Outline each blood parasite and name the species.
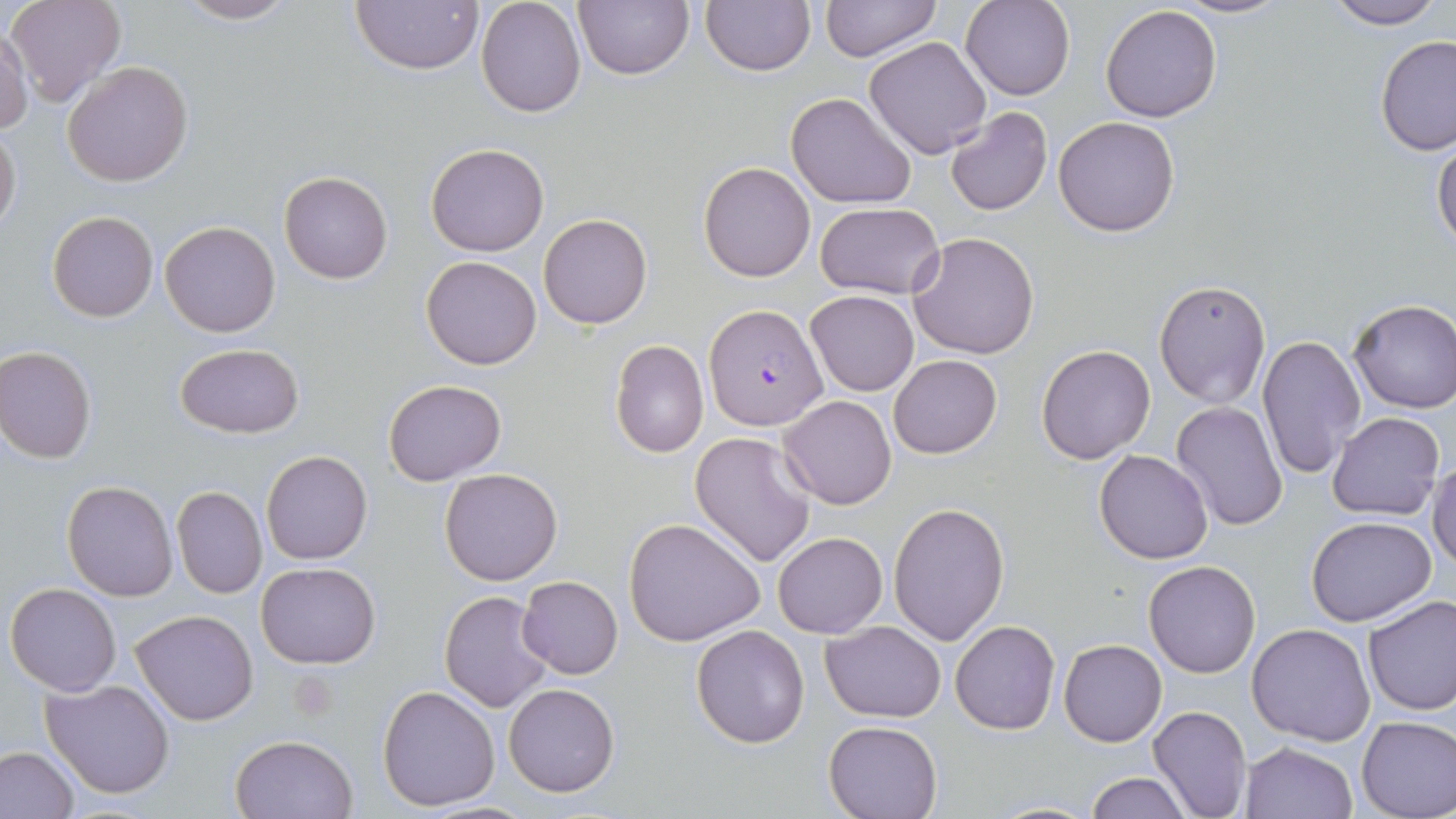

Approximate bounding boxes as (x1, y1, x2, y2) in pixels.
Plasmodium falciparum-infected red blood cells: (704, 305, 827, 430).
No Plasmodium ovale, Plasmodium malariae, Plasmodium vivax, Babesia divergens, or Trypanosoma brucei observed.

{
  "slide_level_diagnosis": "Plasmodium falciparum",
  "field_of_view": "one of a larger specimen",
  "preparation": "thin blood smear",
  "image_size": "1456×819 pixels",
  "uninfected_red_blood_cell_locations": "approximate bounding boxes as (x1, y1, x2, y2) in pixels: (7, 0, 127, 108), (173, 0, 302, 25), (573, 0, 693, 81), (701, 0, 816, 77), (819, 0, 943, 64), (960, 0, 1073, 100), (1169, 0, 1293, 19), (1323, 0, 1447, 29), (350, 1, 484, 76), (475, 1, 586, 118), (1099, 5, 1223, 123), (0, 28, 32, 132), (1376, 35, 1456, 157), (865, 36, 991, 159), (63, 60, 193, 186), (785, 92, 914, 209), (944, 107, 1052, 216), (1053, 116, 1181, 237), (0, 125, 21, 232), (1432, 136, 1456, 257), (426, 142, 548, 256), (699, 161, 815, 281), (279, 171, 393, 285), (814, 201, 946, 299), (48, 211, 159, 323), (539, 213, 652, 328), (160, 220, 280, 337), (908, 232, 1039, 359), (421, 255, 543, 370), (1154, 280, 1270, 407), (806, 291, 918, 396), (1347, 298, 1456, 413), (1256, 335, 1366, 477), (610, 339, 708, 458), (175, 343, 305, 439), (1036, 344, 1156, 464), (0, 346, 97, 463), (888, 354, 1001, 459), (383, 380, 507, 485), (779, 393, 896, 510), (1171, 402, 1288, 533), (1328, 411, 1444, 520), (689, 431, 818, 568), (1095, 449, 1213, 564), (261, 450, 372, 565), (1430, 455, 1456, 573), (439, 467, 565, 586), (61, 480, 178, 601), (171, 485, 267, 598), (889, 501, 1011, 646), (1306, 515, 1437, 625), (624, 517, 767, 647), (773, 532, 888, 639), (1143, 561, 1261, 679), (257, 563, 381, 668), (516, 575, 622, 679), (6, 582, 123, 697), (440, 590, 557, 712), (1362, 594, 1456, 715), (131, 609, 258, 725), (820, 620, 946, 723), (951, 620, 1060, 736), (1248, 623, 1375, 746), (691, 625, 809, 748), (1059, 640, 1166, 747), (42, 675, 177, 800), (377, 683, 501, 812), (504, 683, 619, 797), (1148, 705, 1252, 819), (1356, 715, 1456, 818), (823, 719, 944, 819), (230, 733, 358, 819), (1241, 741, 1358, 819), (0, 746, 82, 819), (1086, 773, 1193, 818), (987, 801, 1102, 817)",
  "stain": "May-Grünwald-Giemsa",
  "modality": "optical microscopy",
  "magnification": "1000x"
}